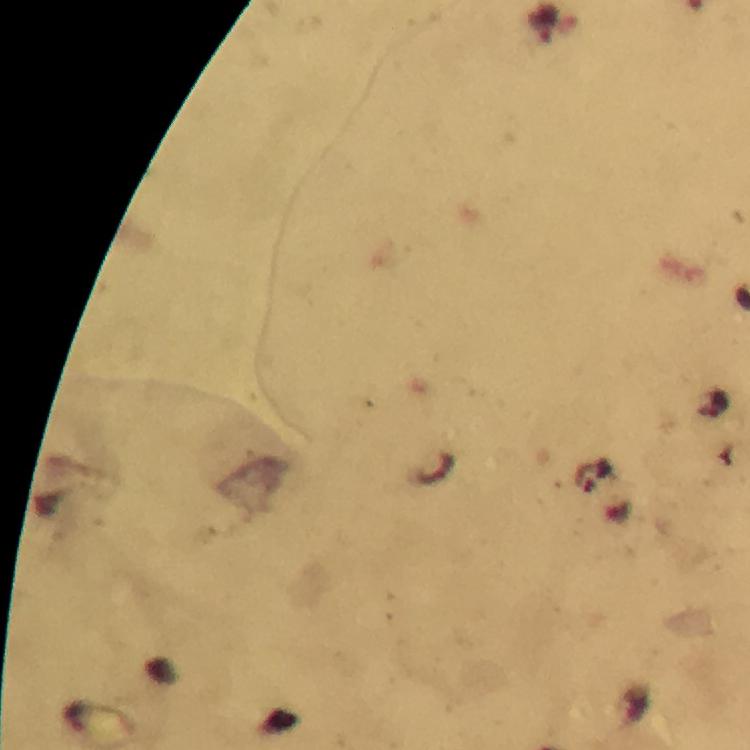 Approximate centers as (x, y) in pixels. Malaria parasite locations: (542, 26). Photographed through the microscope with a smartphone camera. Image is 750×750 pixels. 100x magnification. Giemsa stain. Immersion oil applied. Thick blood film. A crop from one field of view. From a diagnostic examination for malaria.